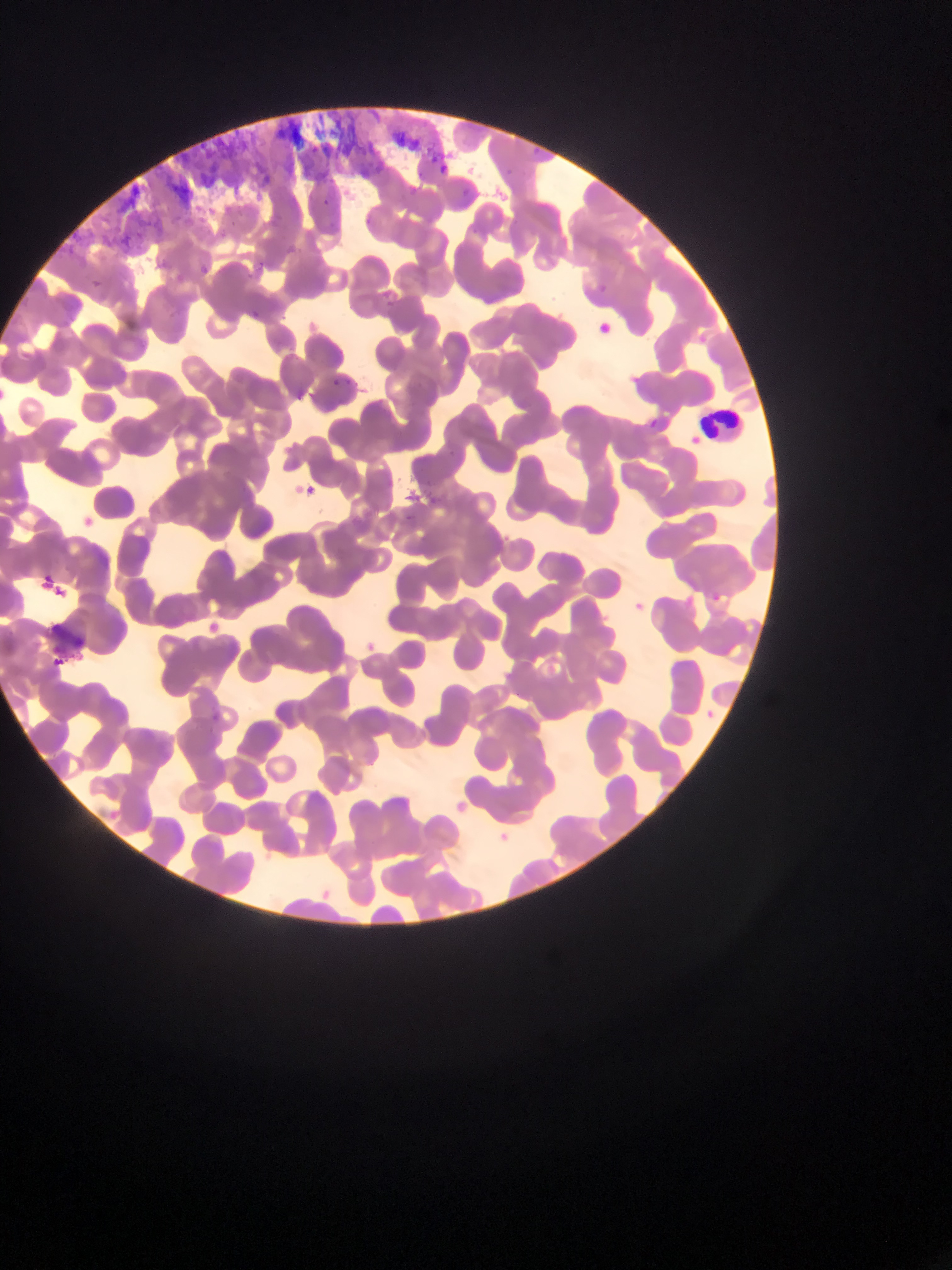
preparation = thin blood film
field of view = single
capture = mobile-phone photograph through a microscope
image size = 952×1270 pixels
leukocyte locations = approximate bounding boxes as left top right bottom in pixels: 703 404 745 443
artifact (stain precipitate or debris) locations = approximate bounding boxes as left top right bottom in pixels: 49 623 100 658
malaria parasite locations = approximate bounding boxes as left top right bottom in pixels: 323 194 334 213; 592 318 613 336; 329 378 341 386; 653 410 662 424; 301 477 322 500; 79 514 100 534; 41 573 68 611; 712 589 721 603; 635 597 645 610; 201 615 225 638; 363 635 380 655; 706 706 718 724; 209 709 222 723 | approximate x y pixel centers of objects too small to bound: 466 188
country = Ghana